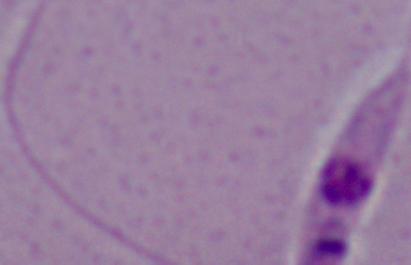

identification = Leishmania
modality = micrograph
magnification = 1000x